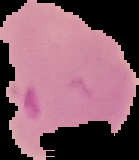 Result: malaria parasites identified. From a thin blood film. Image is 139×160 pixels. Cell region segmented out of the field of view; the surrounding area is masked to black.